Give the extent of all Plasmodium vivax-infected red blood cells.
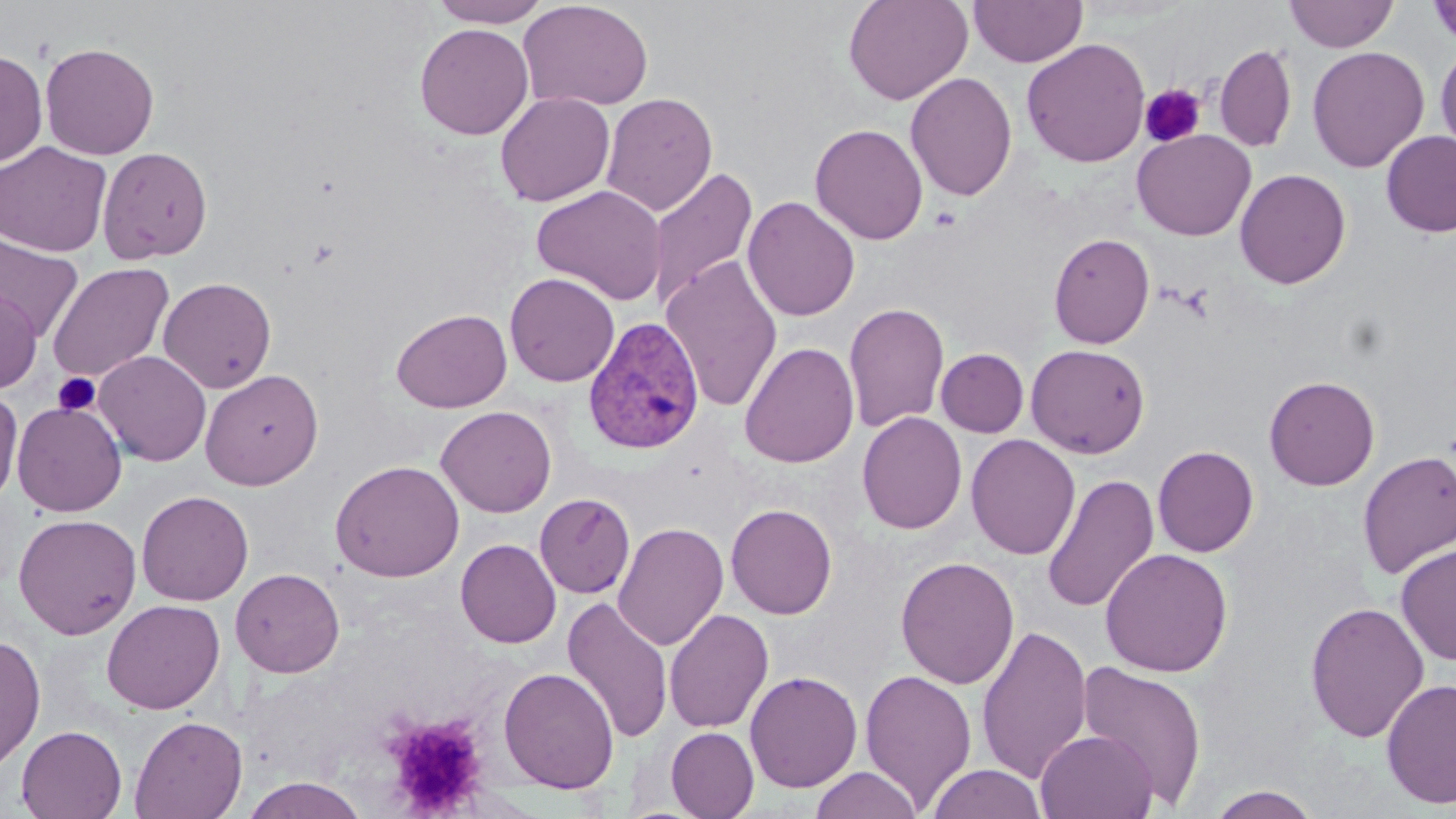
Approximate bounding boxes as named x1/y1/x2/y2 corners in pixels.
Plasmodium vivax-infected red blood cells: (x1=583, y1=317, x2=705, y2=455).

Summary:
  - Uninfected red blood cell locations: (x1=429, y1=0, x2=551, y2=27), (x1=517, y1=0, x2=654, y2=112), (x1=843, y1=0, x2=973, y2=105), (x1=969, y1=0, x2=1088, y2=67), (x1=1285, y1=0, x2=1398, y2=52), (x1=1428, y1=1, x2=1456, y2=49), (x1=414, y1=23, x2=535, y2=140), (x1=1021, y1=38, x2=1151, y2=167), (x1=40, y1=42, x2=159, y2=160), (x1=1435, y1=42, x2=1456, y2=158), (x1=1214, y1=44, x2=1296, y2=152), (x1=1307, y1=45, x2=1430, y2=173), (x1=0, y1=49, x2=48, y2=168), (x1=905, y1=71, x2=1017, y2=202), (x1=494, y1=92, x2=615, y2=206), (x1=601, y1=92, x2=718, y2=217), (x1=810, y1=123, x2=928, y2=245), (x1=1132, y1=129, x2=1255, y2=241), (x1=1381, y1=130, x2=1456, y2=237), (x1=0, y1=141, x2=112, y2=257), (x1=97, y1=146, x2=213, y2=264), (x1=648, y1=167, x2=758, y2=310), (x1=1234, y1=168, x2=1351, y2=289), (x1=531, y1=185, x2=667, y2=305), (x1=743, y1=196, x2=860, y2=322), (x1=1049, y1=232, x2=1155, y2=349), (x1=0, y1=236, x2=84, y2=341), (x1=660, y1=254, x2=783, y2=412), (x1=47, y1=262, x2=174, y2=384), (x1=504, y1=273, x2=620, y2=387), (x1=158, y1=276, x2=277, y2=393), (x1=0, y1=289, x2=42, y2=394), (x1=843, y1=302, x2=950, y2=434), (x1=391, y1=308, x2=512, y2=413), (x1=739, y1=342, x2=860, y2=468), (x1=1026, y1=344, x2=1150, y2=458), (x1=936, y1=348, x2=1029, y2=437), (x1=94, y1=351, x2=211, y2=466), (x1=200, y1=369, x2=324, y2=490), (x1=1264, y1=374, x2=1380, y2=490), (x1=0, y1=387, x2=23, y2=508), (x1=11, y1=401, x2=127, y2=517), (x1=436, y1=406, x2=556, y2=517), (x1=857, y1=411, x2=967, y2=534), (x1=966, y1=434, x2=1081, y2=560), (x1=1152, y1=445, x2=1259, y2=557), (x1=1357, y1=450, x2=1456, y2=580), (x1=330, y1=460, x2=465, y2=582), (x1=1042, y1=473, x2=1159, y2=614), (x1=136, y1=490, x2=253, y2=606), (x1=535, y1=494, x2=635, y2=598), (x1=726, y1=503, x2=837, y2=619), (x1=12, y1=513, x2=142, y2=640), (x1=612, y1=522, x2=729, y2=652), (x1=456, y1=539, x2=561, y2=648), (x1=1395, y1=544, x2=1456, y2=666), (x1=1100, y1=548, x2=1233, y2=677), (x1=895, y1=556, x2=1020, y2=689), (x1=230, y1=568, x2=345, y2=678), (x1=562, y1=596, x2=673, y2=744), (x1=102, y1=599, x2=225, y2=714), (x1=1304, y1=600, x2=1429, y2=743), (x1=664, y1=608, x2=774, y2=733), (x1=976, y1=624, x2=1092, y2=784), (x1=0, y1=633, x2=46, y2=773), (x1=1075, y1=661, x2=1209, y2=808), (x1=498, y1=667, x2=619, y2=794), (x1=859, y1=668, x2=978, y2=811), (x1=744, y1=670, x2=863, y2=793), (x1=1381, y1=677, x2=1456, y2=809), (x1=129, y1=715, x2=247, y2=819), (x1=16, y1=724, x2=127, y2=818), (x1=665, y1=727, x2=759, y2=818), (x1=1036, y1=729, x2=1158, y2=819), (x1=926, y1=764, x2=1048, y2=819), (x1=809, y1=766, x2=923, y2=819), (x1=239, y1=776, x2=369, y2=818), (x1=1206, y1=786, x2=1321, y2=818)
  - Platelet locations: (x1=1140, y1=84, x2=1207, y2=147), (x1=53, y1=372, x2=101, y2=416), (x1=385, y1=714, x2=489, y2=816)
  - Slide-level diagnosis: Plasmodium vivax
  - Image size: 1456×819 pixels
  - Field of view: one of a larger specimen
  - Preparation: thin blood smear
  - Magnification: 1000x
  - Modality: optical microscopy
  - Stain: May-Grünwald-Giemsa